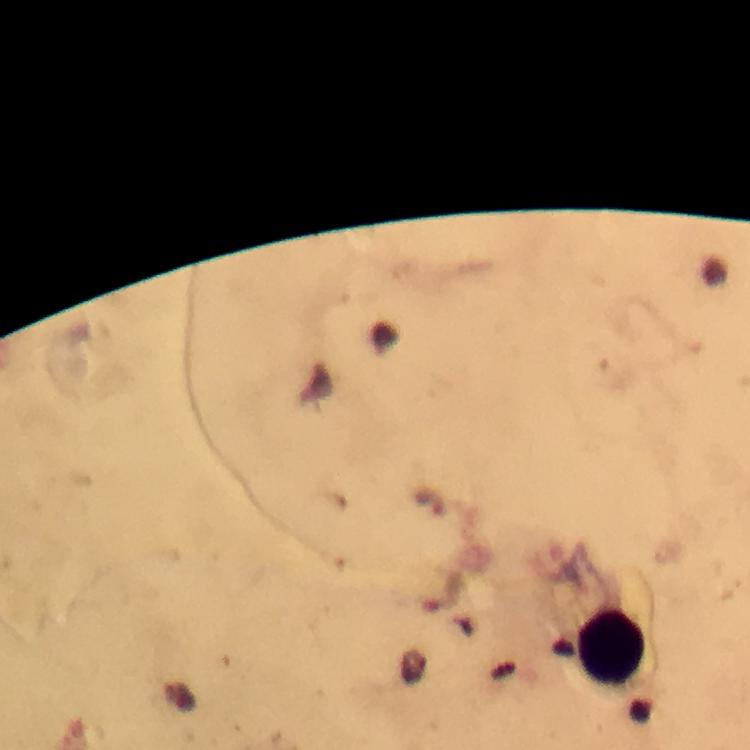

Approximate centers as [x, y] in pixels. Leukocyte locations: [610, 646]. A crop from one field of view. Immersion oil was used. Image is 750×750 pixels. Photographed with a smartphone mounted on the microscope. From a malaria diagnostic workup. 100x magnification. Thick blood smear. Giemsa-stained preparation. Plasmodium parasites: none seen.